Mark where platelets are.
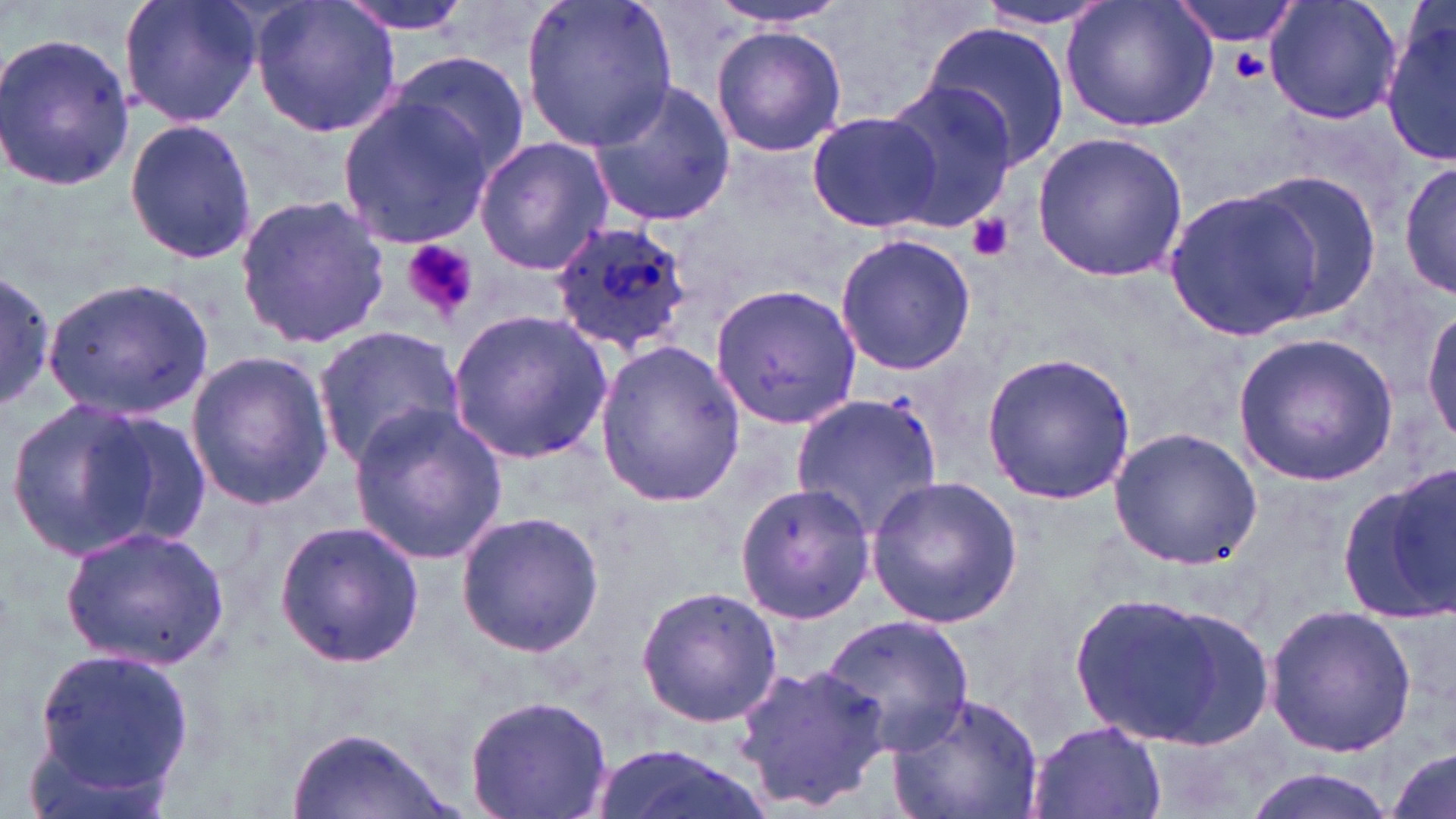
Approximate bounding boxes as (x1, y1, x2, y2) in pixels.
Platelets: (1227, 49, 1273, 82), (967, 214, 1015, 262), (402, 240, 478, 319).

Summary:
  - Uninfected red blood cell locations: (117, 0, 264, 129), (250, 0, 404, 139), (334, 0, 476, 35), (520, 0, 678, 151), (700, 0, 862, 29), (1060, 0, 1219, 135), (1168, 0, 1310, 48), (1264, 0, 1402, 127), (972, 2, 1124, 30), (1380, 11, 1456, 165), (919, 22, 1069, 171), (710, 23, 847, 157), (0, 29, 134, 193), (384, 50, 528, 181), (878, 79, 1018, 230), (586, 82, 737, 227), (335, 96, 497, 249), (807, 109, 949, 236), (120, 119, 259, 266), (1031, 131, 1188, 282), (475, 135, 612, 276), (1399, 159, 1456, 303), (1240, 170, 1385, 322), (1162, 184, 1329, 339), (232, 191, 390, 351), (833, 233, 976, 376), (0, 267, 55, 414), (45, 278, 214, 417), (709, 282, 862, 430), (448, 310, 612, 463), (1422, 311, 1456, 450), (313, 325, 467, 468), (1234, 332, 1401, 484), (593, 340, 744, 508), (980, 348, 1136, 506), (184, 349, 336, 513), (790, 391, 947, 538), (4, 397, 171, 562), (348, 403, 507, 567), (90, 410, 215, 551), (1107, 427, 1260, 567), (1344, 472, 1455, 621), (865, 476, 1023, 626), (735, 481, 878, 624), (455, 511, 606, 659), (272, 518, 425, 670), (60, 523, 230, 671), (634, 585, 783, 727), (1064, 588, 1240, 744), (1262, 604, 1418, 757), (1134, 605, 1274, 751), (822, 614, 975, 756), (32, 646, 194, 798), (730, 658, 892, 811), (887, 692, 1045, 819), (464, 694, 613, 819), (1027, 720, 1167, 819), (286, 727, 454, 819), (591, 743, 764, 819), (1384, 746, 1455, 818), (1243, 769, 1399, 819)
  - Plasmodium ovale-infected red blood cell locations: (549, 219, 696, 358)
  - Slide-level diagnosis: Plasmodium ovale
  - Stain: May-Grünwald-Giemsa
  - Image size: 1456×819 pixels
  - Magnification: 1000x
  - Modality: optical microscopy
  - Preparation: thin blood film
  - Field of view: single